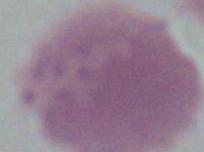

An erythrocyte is shown. 1000x magnification. Photomicrograph.